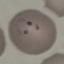
Summary:
  - Result: malaria parasites detected
  - Preparation: thin blood smear
  - Stain: Giemsa
  - Image type: automatically extracted cell patch, resized to 64 × 64 pixels
  - Capture: smartphone camera at the microscope eyepiece